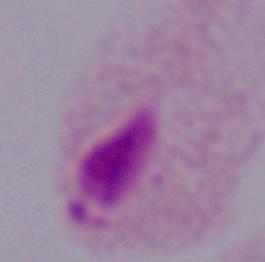

Captured at 1000x magnification. A trichomonad is shown. Micrograph.